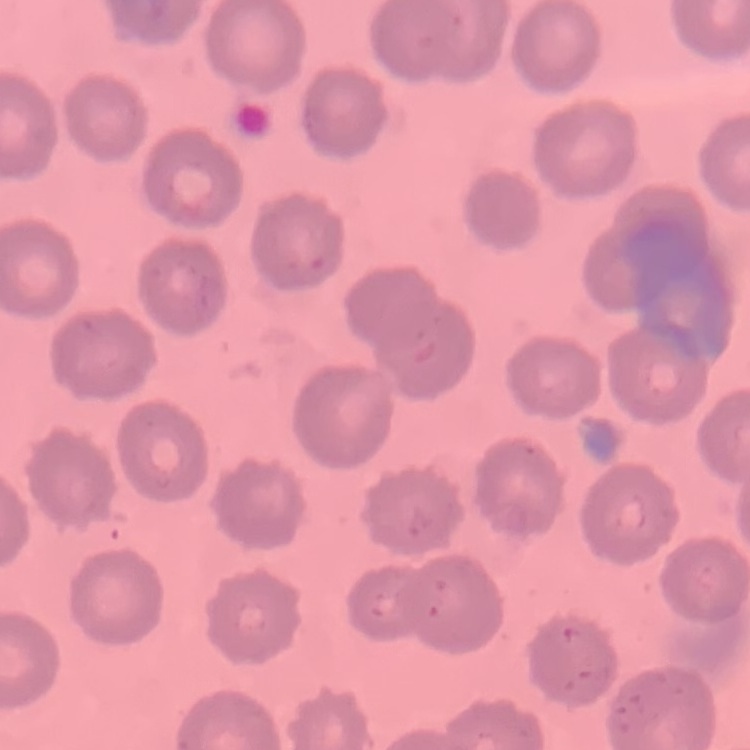

The red blood cells show no rouleaux formation. Square crop of a larger photomicrograph. Thin peripheral smear. Field's or Giemsa stain.